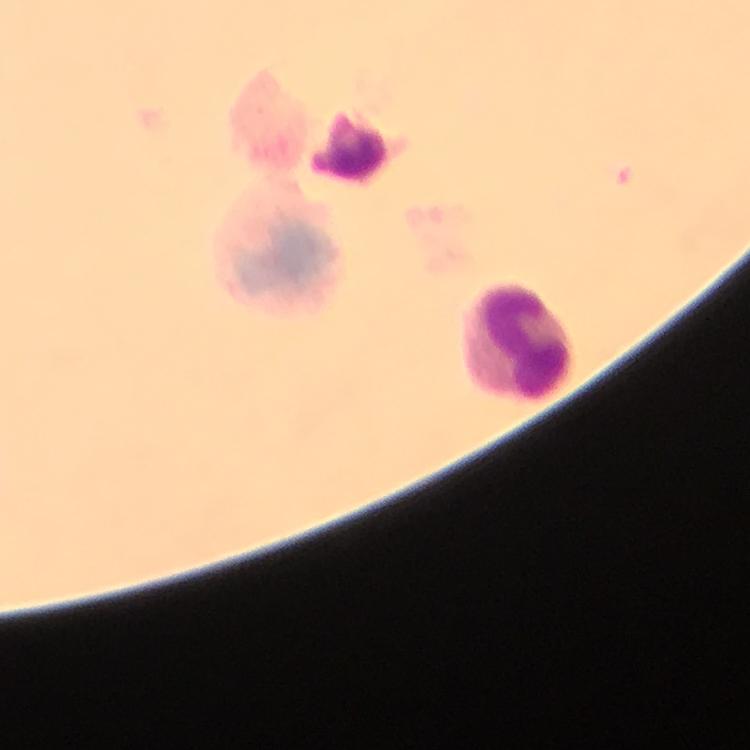
capture = smartphone mounted on the microscope
cropped from = one field of view
Plasmodium parasites = none detected
magnification = 100x
preparation = thick blood film
leukocyte locations = approximate object centers, in pixels from the top-left corner: (x=279, y=249), (x=519, y=336)
immersion oil = used
context = from a malaria diagnostic workup
stain = Giemsa
image size = 750×750 pixels